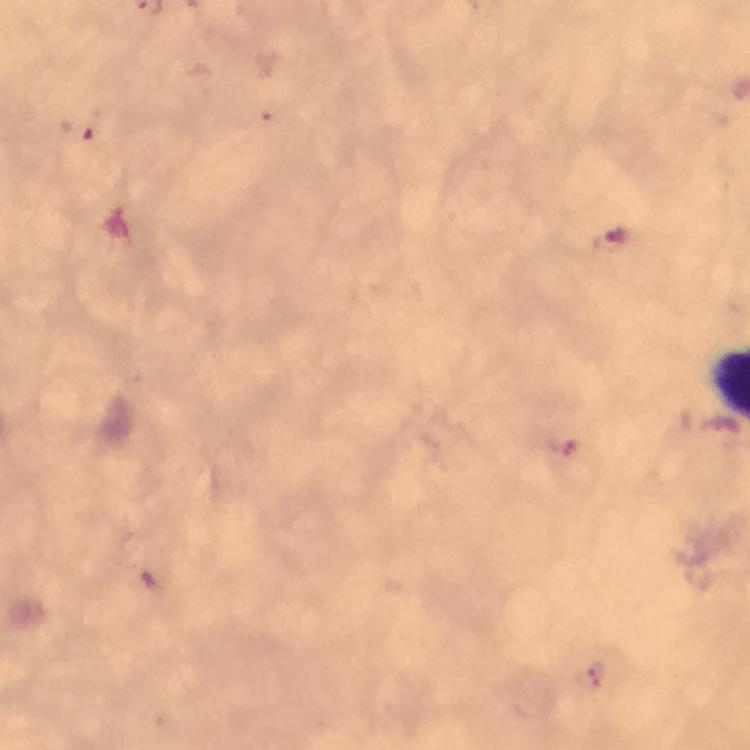

context = from a malaria diagnostic workup
preparation = thick blood film
Plasmodium parasite locations = approximate centers as [x, y] in pixels: [83, 131], [613, 242], [561, 445], [593, 677]
image size = 750×750 pixels
capture = smartphone photograph through a microscope
immersion oil = applied
magnification = 100x
cropped from = a single field of view
stain = Giemsa